Classify this cell by malaria status.
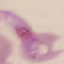

It is parasitized.

preparation = thin blood smear
stain = Giemsa
image type = automatically extracted cell patch, resized to 64 × 64 pixels
capture = smartphone camera at the microscope eyepiece